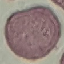

Summary:
  - Result: no malaria parasites seen
  - Stain: Giemsa
  - Image type: automatically extracted cell patch, resized to 64 × 64 pixels
  - Preparation: thin blood film
  - Capture: smartphone through the microscope eyepiece